Locate every blood parasite and identify its species.
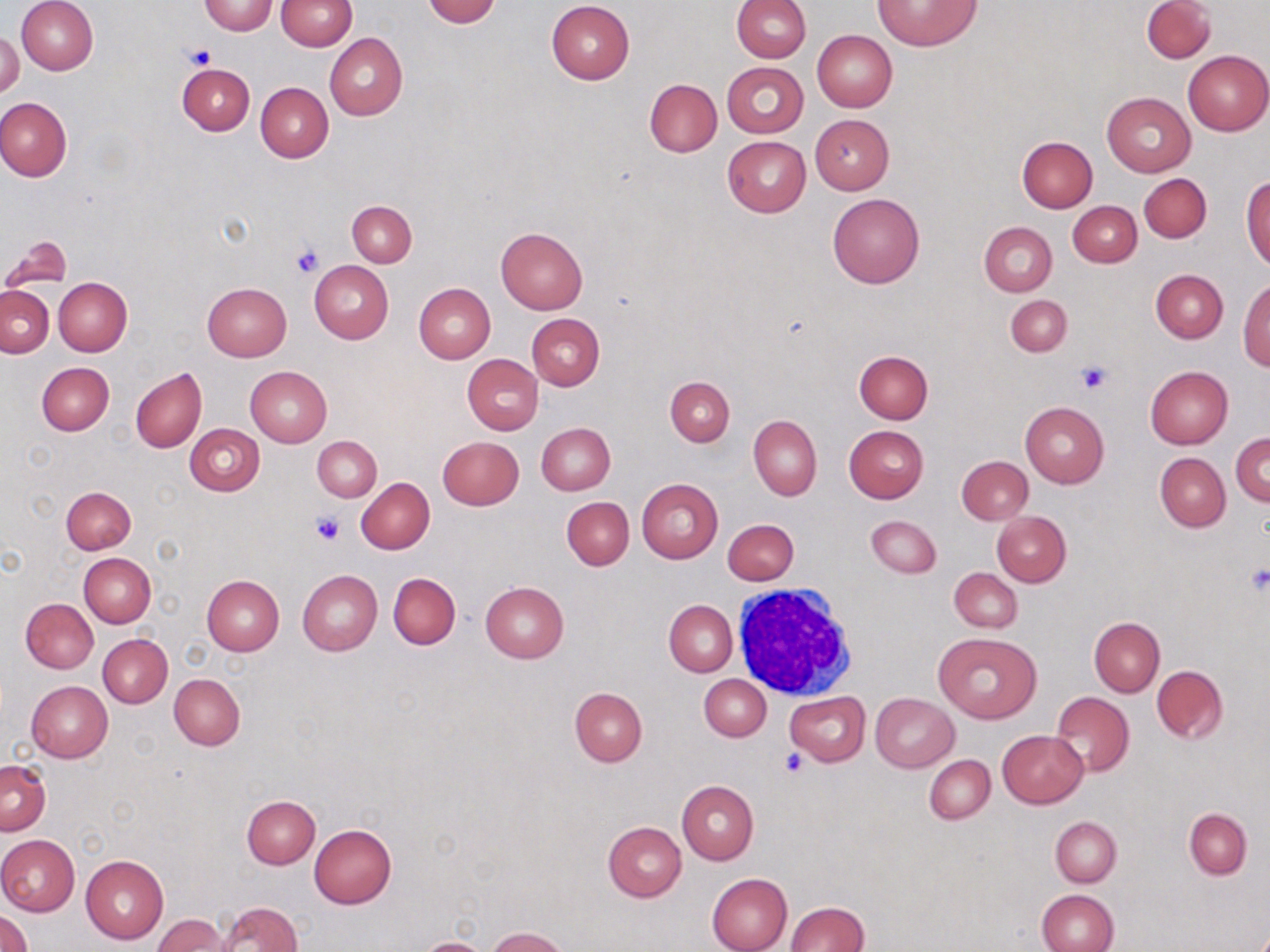

No blood parasites seen.

Summary:
  - Coordinate format: approximate bounding boxes as (x1,y1)-(x2,y2) corner pairs in pixels
  - Platelet locations: (187,45)-(215,70), (290,243)-(324,279), (1075,361)-(1113,394), (311,513)-(346,544), (1243,566)-(1270,595), (779,748)-(810,778)
  - White blood cell locations: (730,582)-(861,700)
  - Uninfected red blood cell locations: (17,0)-(98,75), (275,0)-(355,51), (422,0)-(502,26), (732,0)-(810,63), (875,0)-(981,50), (1142,0)-(1215,62), (198,1)-(277,35), (546,1)-(635,84), (0,30)-(23,99), (812,30)-(897,112), (325,33)-(408,120), (1183,49)-(1270,135), (177,61)-(254,134), (723,62)-(808,137), (645,79)-(721,157), (256,82)-(332,162), (1101,91)-(1196,177), (0,97)-(73,181), (810,114)-(894,194), (722,136)-(811,217), (1017,136)-(1097,212), (1139,174)-(1211,243), (1242,177)-(1270,268), (828,193)-(924,289), (348,201)-(416,267), (1069,201)-(1142,266), (980,222)-(1058,296), (495,226)-(587,313), (1,236)-(71,291), (309,261)-(393,343), (1150,270)-(1228,343), (53,277)-(131,356), (1238,280)-(1270,371), (202,282)-(292,361), (414,282)-(495,362), (0,286)-(53,357), (1005,295)-(1072,356), (527,314)-(605,391), (854,350)-(933,423), (463,355)-(542,435), (451,357)-(531,513), (37,363)-(113,436), (1145,366)-(1234,449), (246,367)-(332,447), (131,368)-(206,453), (664,376)-(735,445), (1020,401)-(1109,487), (749,415)-(822,501), (537,422)-(615,495), (548,422)-(622,569), (186,423)-(264,496), (844,426)-(928,503), (1231,432)-(1270,506), (312,436)-(381,502), (437,436)-(524,509), (1156,452)-(1230,531), (957,455)-(1032,524), (356,478)-(434,554), (636,478)-(723,563), (70,485)-(142,625), (61,486)-(135,554), (561,497)-(634,570), (992,512)-(1071,587), (866,515)-(941,578), (724,519)-(798,584), (79,553)-(155,627), (950,567)-(1021,633), (297,569)-(382,656), (388,573)-(460,649), (201,574)-(284,655), (481,582)-(568,663), (20,598)-(98,674), (665,600)-(737,676), (1089,618)-(1164,696), (933,631)-(1042,724), (99,634)-(172,708), (1151,665)-(1228,744), (169,673)-(245,750), (699,675)-(771,740), (25,680)-(113,762), (570,687)-(647,765), (785,691)-(869,765), (1050,691)-(1133,777), (871,693)-(959,773), (997,730)-(1088,808), (926,745)-(1084,814), (925,755)-(995,824), (1,759)-(50,835), (677,780)-(759,864), (242,795)-(321,868), (1184,809)-(1251,879), (1050,816)-(1121,887), (603,821)-(686,901), (309,824)-(397,909), (0,834)-(79,916), (79,855)-(168,945), (707,873)-(792,952), (1036,889)-(1117,952), (216,901)-(303,951), (786,901)-(870,952), (1,909)-(34,952), (153,915)-(228,952), (488,927)-(569,952), (419,938)-(490,952)
  - Slide-level diagnosis: negative for blood parasites
  - Field of view: one of a larger specimen
  - Preparation: thin blood film
  - Modality: light microscopy
  - Magnification: 1000x
  - Image size: 1270×952 pixels
  - Stain: May-Grünwald-Giemsa